Comment on the morphology of the erythrocytes.
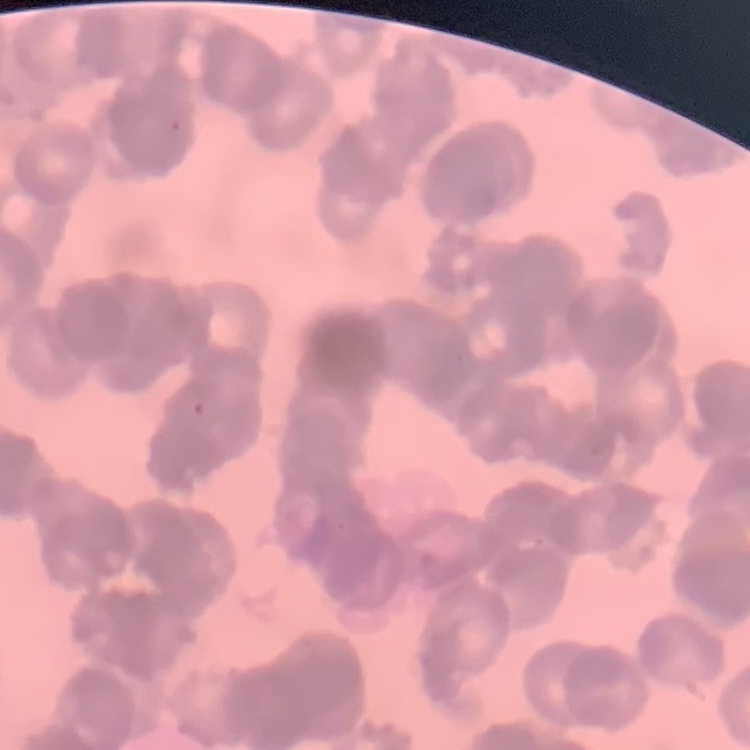

They show rouleaux formation.

stain = Field's or Giemsa
image type = square crop of a larger photomicrograph
preparation = thin blood smear